Classify this cell by malaria status.
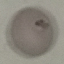

Parasitized.

Summary:
  - Preparation: thin smear
  - Capture: smartphone through the microscope eyepiece
  - Stain: Giemsa
  - Image type: automatically extracted cell patch, resized to 64 × 64 pixels